Classify this cell by malaria status.
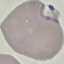

Parasitized.

Cell patch, automatically extracted from a larger field of view and resized to 64 × 64 pixels. Giemsa stain. Acquired by smartphone through the microscope eyepiece. Thin blood smear.